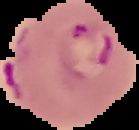

Result: Plasmodium parasites detected. The area outside the segmented cell region is set to black. From a thin blood smear. Image is 139×130 pixels.